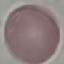

result: no malaria parasites detected
stain: Giemsa
image_type: automatically extracted cell patch, resized to 64 × 64 pixels
capture: smartphone camera at the microscope eyepiece
preparation: thin blood film